Comment on the morphology of the erythrocytes.
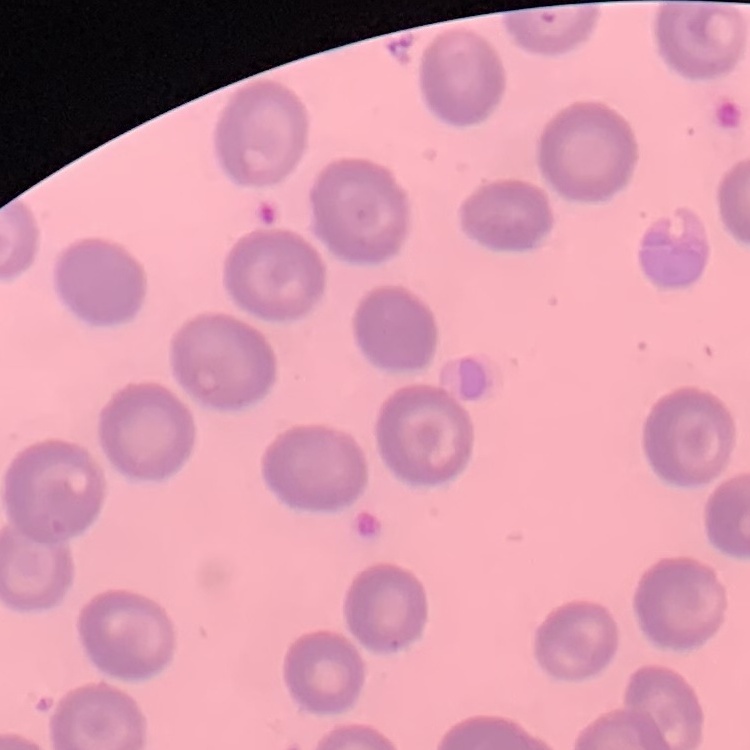

No rouleaux formation.

stain = Field's or Giemsa
preparation = thin blood film
image type = one tile cut from a larger photomicrograph